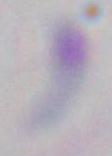

Toxoplasma gondii is shown. 1000x magnification. Micrograph.